Assess this cell for malaria.
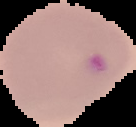
Parasitized.

From a thin blood smear. Cell region segmented out of the field of view; the surrounding area is masked to black. Image is 136×127 pixels.